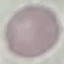
result = no malaria parasites detected
image type = cell patch, automatically extracted from a larger field of view and resized to 64 × 64 pixels
preparation = thin smear
stain = Giemsa
capture = smartphone camera at the microscope eyepiece